Locate every Plasmodium falciparum-infected red blood cell.
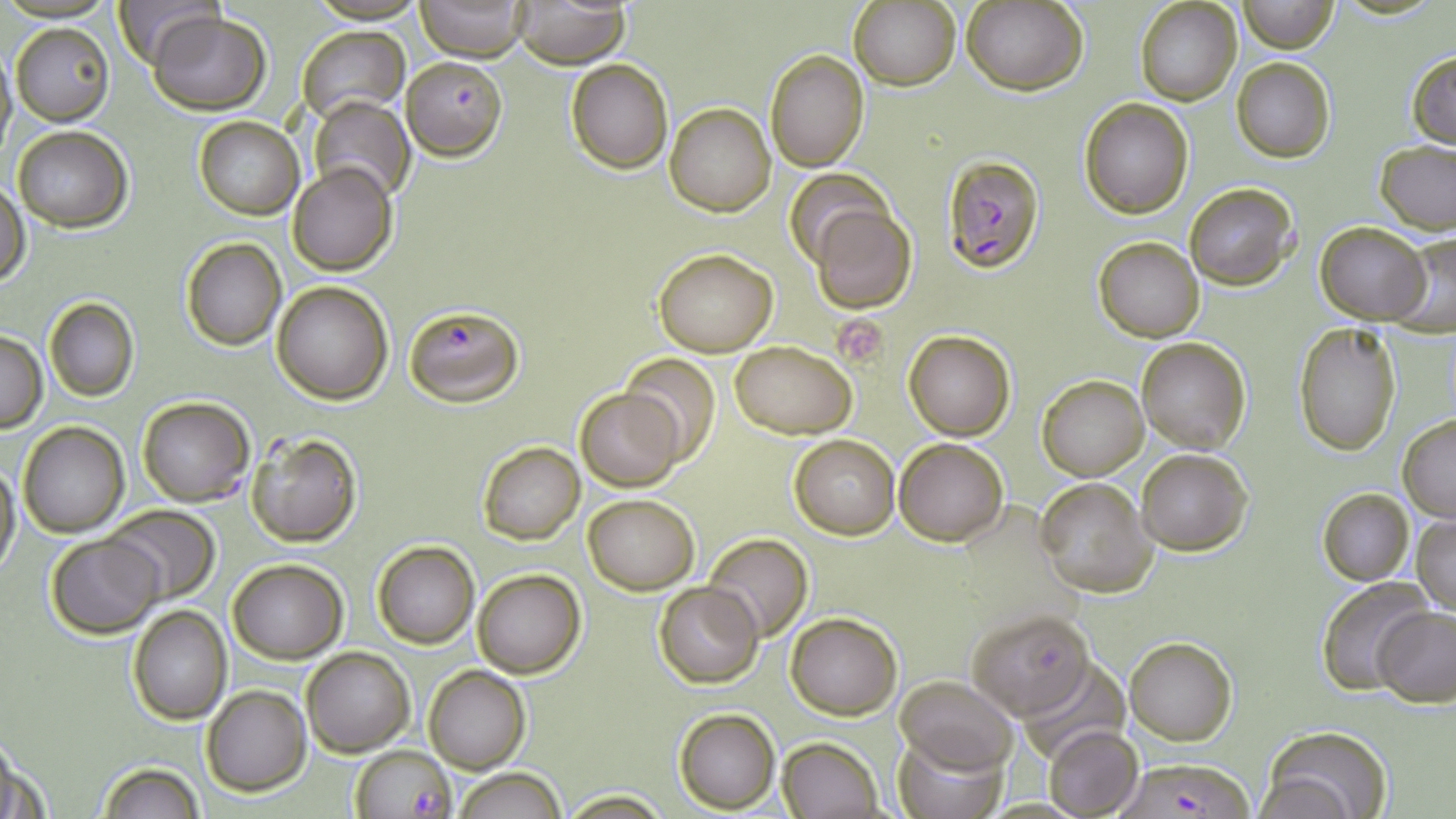
Approximate bounding boxes as named x1/y1/x2/y2 corners in pixels.
Plasmodium falciparum-infected red blood cells (subset): (x1=403, y1=56, x2=507, y2=159), (x1=943, y1=154, x2=1045, y2=273), (x1=403, y1=302, x2=523, y2=405), (x1=966, y1=608, x2=1096, y2=718), (x1=349, y1=745, x2=457, y2=819).

Platelet locations: (x1=835, y1=317, x2=887, y2=372). Uninfected red blood cell locations (subset): (x1=113, y1=0, x2=223, y2=67), (x1=307, y1=0, x2=424, y2=23), (x1=417, y1=0, x2=529, y2=61), (x1=1239, y1=0, x2=1337, y2=53), (x1=848, y1=1, x2=960, y2=91), (x1=963, y1=1, x2=1088, y2=96), (x1=1135, y1=1, x2=1242, y2=106), (x1=514, y1=2, x2=629, y2=67), (x1=148, y1=10, x2=271, y2=113), (x1=10, y1=23, x2=114, y2=126), (x1=297, y1=26, x2=409, y2=122), (x1=0, y1=40, x2=16, y2=160), (x1=765, y1=49, x2=869, y2=171), (x1=1407, y1=49, x2=1456, y2=149), (x1=1232, y1=58, x2=1334, y2=161), (x1=565, y1=59, x2=674, y2=174), (x1=309, y1=95, x2=415, y2=204), (x1=1079, y1=98, x2=1194, y2=220), (x1=665, y1=103, x2=775, y2=217), (x1=193, y1=116, x2=305, y2=219), (x1=12, y1=126, x2=132, y2=231), (x1=1374, y1=140, x2=1455, y2=234), (x1=291, y1=163, x2=396, y2=276), (x1=0, y1=182, x2=28, y2=289), (x1=1184, y1=182, x2=1300, y2=291), (x1=809, y1=203, x2=917, y2=313), (x1=1316, y1=221, x2=1429, y2=324), (x1=1389, y1=232, x2=1456, y2=337), (x1=1094, y1=237, x2=1205, y2=342), (x1=180, y1=238, x2=286, y2=351), (x1=654, y1=248, x2=777, y2=356), (x1=272, y1=280, x2=395, y2=404), (x1=44, y1=297, x2=139, y2=402), (x1=1292, y1=321, x2=1403, y2=457), (x1=903, y1=329, x2=1015, y2=441), (x1=1, y1=331, x2=46, y2=431), (x1=1136, y1=337, x2=1251, y2=453), (x1=729, y1=341, x2=856, y2=437), (x1=619, y1=354, x2=722, y2=465), (x1=1038, y1=375, x2=1148, y2=480), (x1=576, y1=387, x2=683, y2=491), (x1=137, y1=396, x2=255, y2=507), (x1=1398, y1=414, x2=1456, y2=522), (x1=18, y1=422, x2=129, y2=537), (x1=246, y1=431, x2=362, y2=548), (x1=788, y1=433, x2=901, y2=540), (x1=893, y1=437, x2=1008, y2=547), (x1=476, y1=441, x2=586, y2=545), (x1=1135, y1=449, x2=1253, y2=556), (x1=0, y1=460, x2=20, y2=578), (x1=1034, y1=477, x2=1157, y2=597), (x1=1318, y1=488, x2=1414, y2=585), (x1=584, y1=494, x2=700, y2=594), (x1=105, y1=505, x2=220, y2=602), (x1=1412, y1=513, x2=1456, y2=617), (x1=45, y1=534, x2=164, y2=639), (x1=704, y1=535, x2=813, y2=642), (x1=372, y1=541, x2=480, y2=649), (x1=372, y1=556, x2=584, y2=666), (x1=227, y1=559, x2=348, y2=661), (x1=473, y1=569, x2=586, y2=678), (x1=1317, y1=577, x2=1438, y2=696), (x1=655, y1=582, x2=762, y2=688), (x1=128, y1=606, x2=231, y2=725), (x1=1372, y1=606, x2=1456, y2=705), (x1=787, y1=612, x2=902, y2=719), (x1=1125, y1=637, x2=1236, y2=745), (x1=301, y1=647, x2=415, y2=756), (x1=1022, y1=658, x2=1129, y2=764), (x1=424, y1=665, x2=530, y2=773), (x1=896, y1=676, x2=1017, y2=772), (x1=202, y1=685, x2=311, y2=796), (x1=674, y1=708, x2=780, y2=812), (x1=1044, y1=724, x2=1144, y2=818), (x1=1260, y1=726, x2=1395, y2=819), (x1=1, y1=733, x2=37, y2=819), (x1=893, y1=733, x2=1009, y2=819), (x1=778, y1=736, x2=884, y2=818), (x1=96, y1=762, x2=205, y2=819), (x1=457, y1=767, x2=565, y2=819), (x1=559, y1=790, x2=673, y2=818). Slide-level diagnosis: Plasmodium falciparum. Single field of view. Image is 1456×819 pixels. Light microscopy. Thin blood smear. Captured at 1000x magnification. May-Grünwald-Giemsa stain.